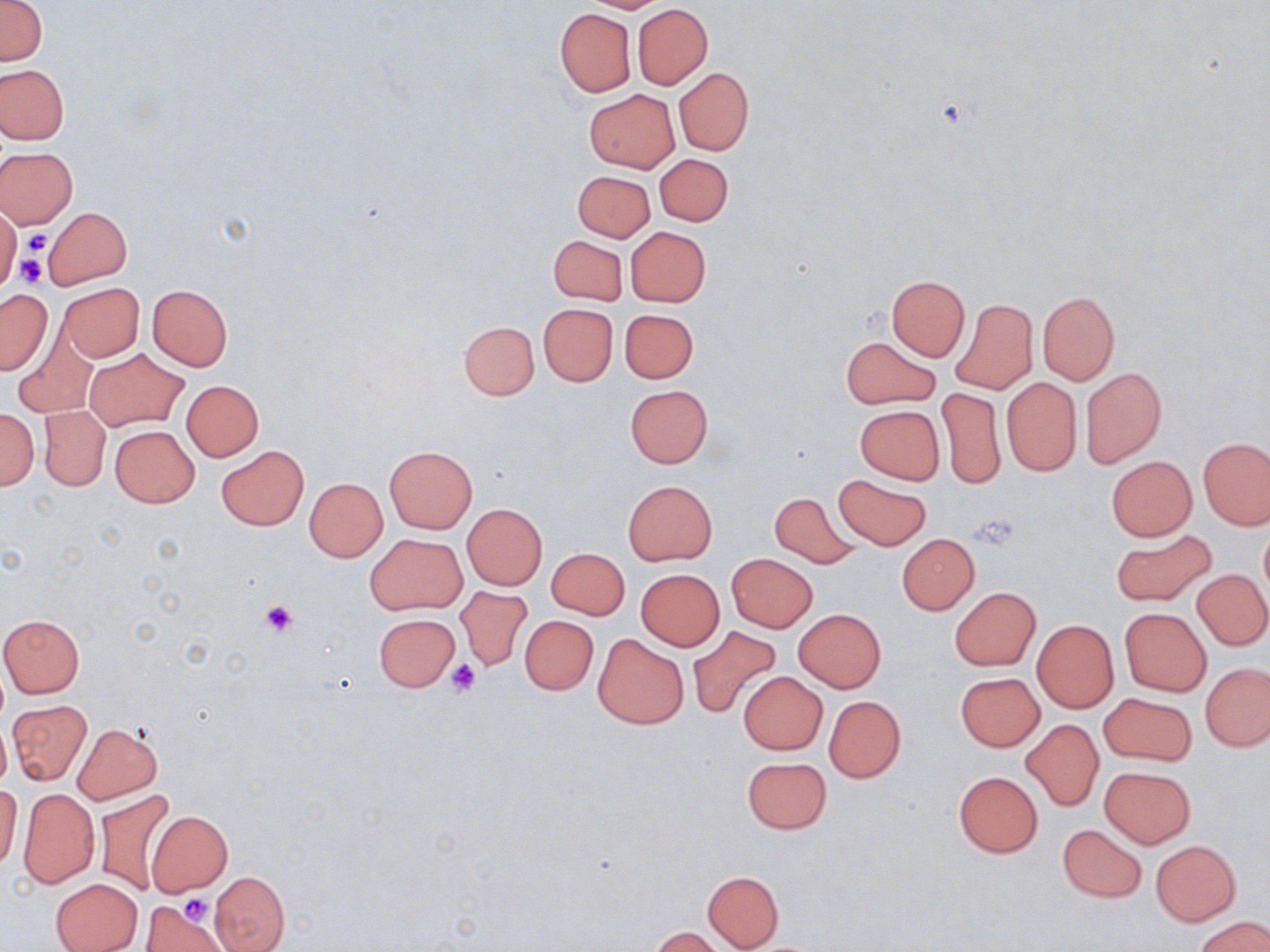
slide-level diagnosis = no evidence of blood parasites
preparation = thin blood smear
magnification = 1000x
uninfected red blood cell locations = approximate bounding boxes as (x1,y1)-(x2,y2) corner pairs in pixels: (0,0)-(47,67), (580,0)-(671,13), (632,4)-(712,88), (555,8)-(636,97), (0,63)-(68,144), (674,68)-(754,154), (584,90)-(679,171), (0,148)-(77,228), (654,153)-(733,225), (573,171)-(654,241), (0,206)-(20,291), (42,208)-(131,288), (625,227)-(711,306), (548,235)-(627,305), (886,275)-(970,360), (58,282)-(143,362), (147,284)-(234,372), (861,286)-(956,399), (0,290)-(51,375), (1037,291)-(1119,384), (950,298)-(1037,395), (538,304)-(617,386), (619,308)-(699,383), (459,321)-(539,400), (15,331)-(96,417), (841,336)-(940,408), (84,348)-(188,431), (1081,366)-(1166,467), (1002,377)-(1082,476), (181,380)-(264,462), (624,384)-(712,468), (938,386)-(1004,490), (854,404)-(945,485), (39,405)-(110,491), (0,408)-(39,490), (109,424)-(199,507), (1199,437)-(1270,529), (216,445)-(308,531), (385,446)-(477,533), (1106,455)-(1196,541), (833,474)-(932,549), (305,478)-(387,561), (622,480)-(717,565), (768,490)-(860,567), (462,503)-(548,589), (1260,527)-(1270,600), (1111,530)-(1217,607), (366,533)-(467,614), (897,533)-(979,614), (546,547)-(629,619), (727,553)-(817,632), (635,569)-(725,650), (1193,569)-(1270,650), (456,586)-(534,671), (949,587)-(1039,671), (1119,608)-(1210,696), (794,609)-(886,692), (373,613)-(460,692), (1,614)-(84,697), (520,615)-(597,695), (1030,619)-(1119,713), (688,626)-(780,718), (593,634)-(688,729), (1201,662)-(1270,751), (739,671)-(827,754), (955,672)-(1045,752), (1099,693)-(1195,766), (823,695)-(906,783), (8,700)-(92,786), (0,717)-(11,795), (1022,718)-(1103,810), (72,722)-(163,804), (740,757)-(832,834), (1099,765)-(1195,848), (953,771)-(1043,858), (0,785)-(23,871), (18,787)-(99,889), (95,789)-(177,896), (146,810)-(233,895), (1057,823)-(1147,901), (1151,840)-(1240,925), (702,870)-(783,950), (209,871)-(289,950), (51,877)-(144,952), (143,899)-(229,950), (1196,916)-(1270,952), (650,927)-(728,952)
stain = May-Grünwald-Giemsa
image size = 1270×952 pixels
field of view = single
platelet locations = approximate bounding boxes as (x1,y1)-(x2,y2) corner pairs in pixels: (20,228)-(53,258), (15,254)-(48,287), (969,510)-(1019,549), (260,597)-(300,639), (446,660)-(480,696), (168,894)-(214,943), (182,894)-(213,924)
modality = light microscopy